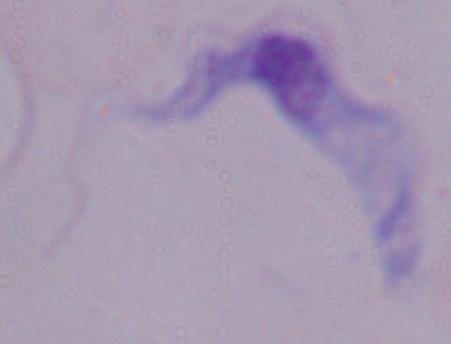
Summary:
  - Magnification: 1000x
  - Modality: photomicrograph
  - Identification: trypanosome